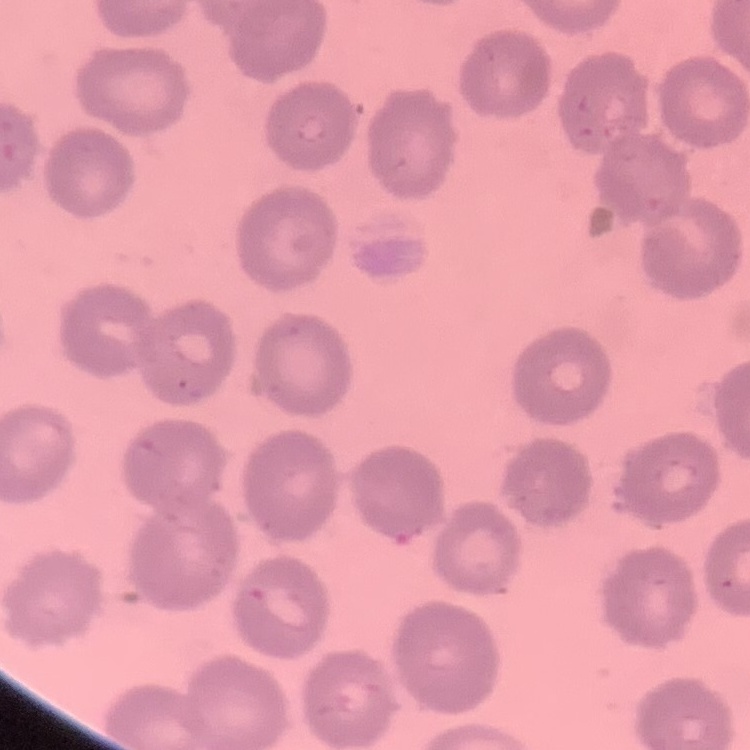
red_blood_cell_morphology: no rouleaux formation
image_type: one tile cut from a larger photomicrograph
stain: Field's or Giemsa
preparation: thin peripheral smear